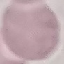

malaria status = uninfected
stain = Giemsa
preparation = thin smear
image type = automatically extracted cell patch, resized to 64 × 64 pixels
capture = smartphone through the microscope eyepiece